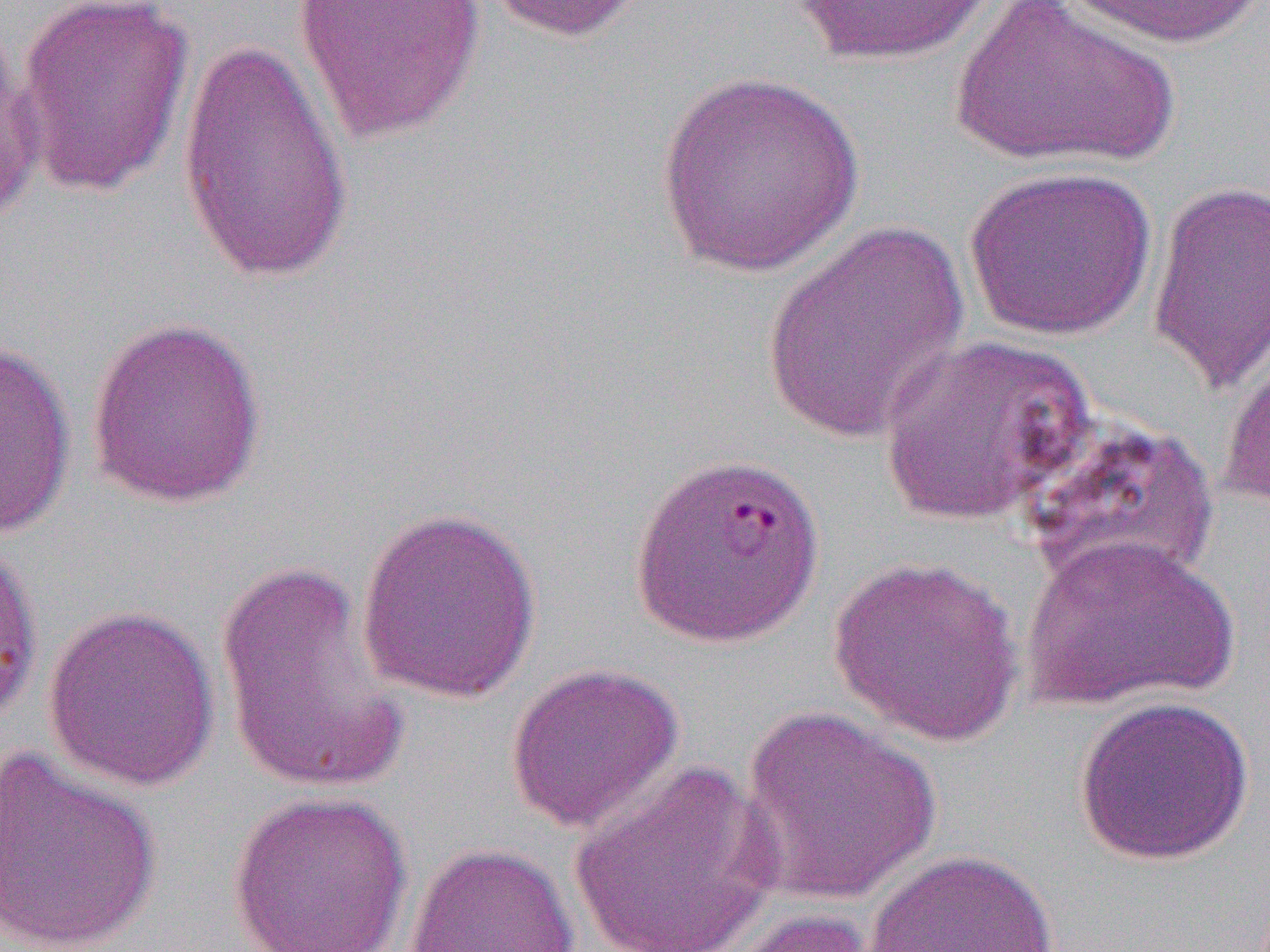

Approximate bounding boxes as named x1/y1/x2/y2 corners in pixels. Uninfected red blood cell locations (subset): (x1=12, y1=0, x2=196, y2=199), (x1=291, y1=0, x2=485, y2=144), (x1=477, y1=0, x2=651, y2=44), (x1=786, y1=0, x2=1003, y2=67), (x1=947, y1=0, x2=1182, y2=172), (x1=1064, y1=0, x2=1264, y2=48), (x1=0, y1=25, x2=44, y2=229), (x1=176, y1=34, x2=356, y2=286), (x1=653, y1=71, x2=864, y2=276), (x1=962, y1=166, x2=1157, y2=341), (x1=1146, y1=179, x2=1269, y2=394), (x1=759, y1=221, x2=972, y2=447), (x1=86, y1=313, x2=269, y2=510), (x1=878, y1=333, x2=1093, y2=526), (x1=1218, y1=339, x2=1270, y2=511), (x1=0, y1=340, x2=77, y2=542), (x1=1019, y1=415, x2=1220, y2=592), (x1=354, y1=505, x2=544, y2=705), (x1=1020, y1=533, x2=1239, y2=712), (x1=0, y1=537, x2=43, y2=727), (x1=829, y1=554, x2=1026, y2=746), (x1=215, y1=560, x2=412, y2=796), (x1=41, y1=604, x2=220, y2=793), (x1=504, y1=662, x2=685, y2=835), (x1=1073, y1=695, x2=1254, y2=867), (x1=736, y1=703, x2=942, y2=905), (x1=0, y1=748, x2=163, y2=952), (x1=566, y1=760, x2=785, y2=952), (x1=227, y1=789, x2=414, y2=952), (x1=403, y1=842, x2=579, y2=951), (x1=863, y1=848, x2=1061, y2=952), (x1=705, y1=907, x2=892, y2=951). Slide-level diagnosis: Plasmodium falciparum. 1000x magnification. Optical microscopy. Thin blood smear. Image is 1270×952 pixels. Single field of view.